Identify the parasite.
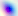
Toxoplasma gondii.

modality: micrograph
magnification: 400x